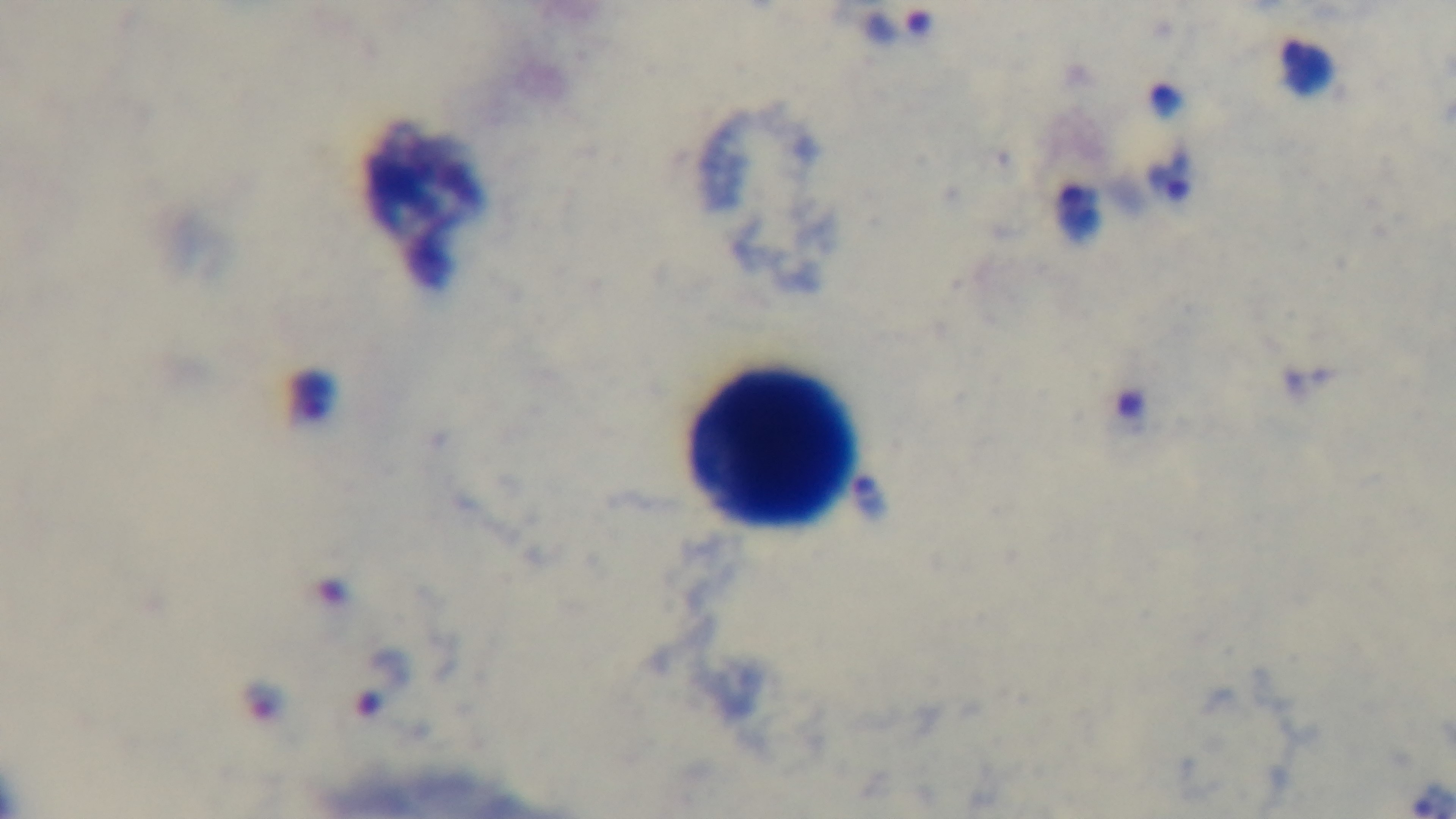
Summary:
  - Objective: 100x oil immersion
  - Capture: mounted 4K digital camera
  - Stain: Giemsa
  - Modality: light microscopy
  - Preparation: thick
  - Malaria status: infected
  - Field of view: one from the slide